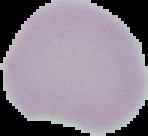

Summary:
  - Image type: segmented cell region with the area outside set to black
  - Preparation: thin blood smear
  - Malaria status: uninfected
  - Image size: 148×136 pixels